Report the malaria status of this cell.
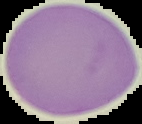
It is uninfected.

image_type: segmented cell region on a black background
preparation: thin blood smear
image_size: 142×124 pixels